Locate every blood parasite and identify its species.
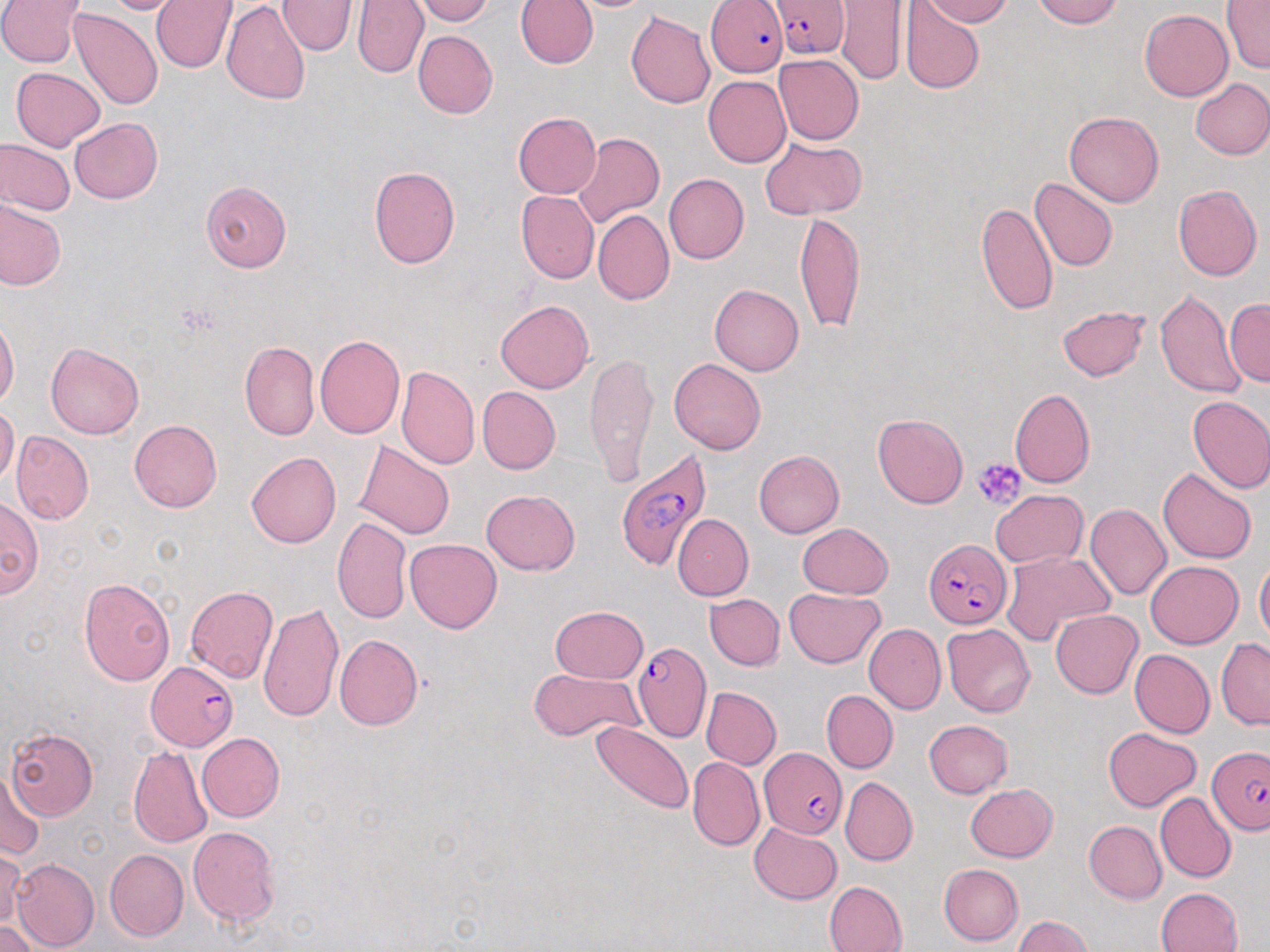
Approximate bounding boxes as named x1/y1/x2/y2 corners in pixels.
Plasmodium falciparum-infected red blood cells: (x1=770, y1=0, x2=849, y2=58), (x1=705, y1=1, x2=788, y2=77), (x1=614, y1=449, x2=712, y2=571), (x1=922, y1=538, x2=1014, y2=630), (x1=632, y1=641, x2=712, y2=742), (x1=143, y1=661, x2=240, y2=751), (x1=1207, y1=744, x2=1270, y2=834), (x1=759, y1=747, x2=845, y2=839).
No Plasmodium ovale, Plasmodium malariae, Plasmodium vivax, Babesia divergens, or Trypanosoma brucei observed.

Summary:
  - Uninfected red blood cell locations: (x1=0, y1=0, x2=84, y2=68), (x1=99, y1=0, x2=188, y2=15), (x1=152, y1=0, x2=237, y2=73), (x1=221, y1=0, x2=311, y2=105), (x1=278, y1=0, x2=359, y2=56), (x1=352, y1=0, x2=429, y2=78), (x1=412, y1=0, x2=493, y2=24), (x1=516, y1=0, x2=598, y2=69), (x1=920, y1=0, x2=1012, y2=27), (x1=1032, y1=0, x2=1120, y2=27), (x1=1220, y1=0, x2=1269, y2=74), (x1=836, y1=1, x2=909, y2=86), (x1=899, y1=1, x2=984, y2=95), (x1=68, y1=6, x2=163, y2=110), (x1=1140, y1=9, x2=1232, y2=101), (x1=626, y1=11, x2=716, y2=109), (x1=413, y1=30, x2=497, y2=119), (x1=774, y1=54, x2=865, y2=144), (x1=11, y1=67, x2=105, y2=150), (x1=703, y1=76, x2=792, y2=168), (x1=1191, y1=78, x2=1270, y2=160), (x1=1065, y1=111, x2=1163, y2=207), (x1=512, y1=112, x2=602, y2=199), (x1=70, y1=117, x2=162, y2=203), (x1=572, y1=132, x2=663, y2=228), (x1=0, y1=137, x2=75, y2=215), (x1=759, y1=137, x2=866, y2=219), (x1=368, y1=166, x2=461, y2=269), (x1=663, y1=173, x2=749, y2=264), (x1=1029, y1=178, x2=1118, y2=272), (x1=201, y1=181, x2=291, y2=271), (x1=1173, y1=184, x2=1262, y2=280), (x1=516, y1=190, x2=599, y2=284), (x1=0, y1=196, x2=65, y2=290), (x1=975, y1=202, x2=1058, y2=317), (x1=592, y1=209, x2=674, y2=306), (x1=795, y1=212, x2=865, y2=336), (x1=710, y1=284, x2=805, y2=376), (x1=1155, y1=288, x2=1245, y2=399), (x1=495, y1=299, x2=594, y2=393), (x1=1226, y1=300, x2=1270, y2=387), (x1=1056, y1=305, x2=1150, y2=381), (x1=0, y1=317, x2=19, y2=409), (x1=314, y1=335, x2=405, y2=439), (x1=239, y1=340, x2=319, y2=440), (x1=45, y1=343, x2=143, y2=439), (x1=584, y1=348, x2=659, y2=488), (x1=669, y1=358, x2=766, y2=455), (x1=396, y1=366, x2=479, y2=469), (x1=478, y1=386, x2=561, y2=473), (x1=1010, y1=388, x2=1095, y2=488), (x1=1187, y1=395, x2=1270, y2=494), (x1=0, y1=405, x2=19, y2=486), (x1=872, y1=413, x2=968, y2=508), (x1=129, y1=419, x2=223, y2=512), (x1=12, y1=431, x2=93, y2=525), (x1=355, y1=440, x2=456, y2=539), (x1=754, y1=449, x2=844, y2=537), (x1=246, y1=451, x2=341, y2=548), (x1=1158, y1=467, x2=1256, y2=564), (x1=481, y1=488, x2=580, y2=576), (x1=991, y1=489, x2=1088, y2=569), (x1=0, y1=497, x2=42, y2=599), (x1=1086, y1=503, x2=1172, y2=600), (x1=672, y1=514, x2=754, y2=600), (x1=332, y1=516, x2=411, y2=624), (x1=797, y1=523, x2=893, y2=598), (x1=405, y1=538, x2=501, y2=633), (x1=1001, y1=551, x2=1115, y2=644), (x1=1255, y1=556, x2=1270, y2=648), (x1=1145, y1=561, x2=1243, y2=648), (x1=78, y1=577, x2=175, y2=686), (x1=184, y1=586, x2=278, y2=684), (x1=784, y1=588, x2=884, y2=667), (x1=704, y1=593, x2=784, y2=670), (x1=258, y1=601, x2=344, y2=722), (x1=550, y1=605, x2=648, y2=684), (x1=1050, y1=609, x2=1142, y2=698), (x1=864, y1=623, x2=945, y2=714), (x1=943, y1=623, x2=1035, y2=717), (x1=334, y1=635, x2=422, y2=731), (x1=1216, y1=638, x2=1270, y2=729), (x1=1130, y1=649, x2=1214, y2=738), (x1=530, y1=668, x2=643, y2=741), (x1=701, y1=686, x2=781, y2=769), (x1=822, y1=690, x2=897, y2=773), (x1=924, y1=719, x2=1014, y2=798), (x1=591, y1=720, x2=694, y2=816), (x1=1103, y1=726, x2=1201, y2=811), (x1=7, y1=728, x2=97, y2=818), (x1=197, y1=731, x2=285, y2=822), (x1=128, y1=746, x2=212, y2=849), (x1=687, y1=757, x2=763, y2=851), (x1=2, y1=767, x2=46, y2=861), (x1=840, y1=777, x2=918, y2=865), (x1=965, y1=783, x2=1058, y2=861), (x1=1155, y1=792, x2=1236, y2=883), (x1=1083, y1=820, x2=1166, y2=904), (x1=750, y1=822, x2=842, y2=904), (x1=188, y1=826, x2=281, y2=928), (x1=0, y1=847, x2=24, y2=929), (x1=104, y1=848, x2=189, y2=941), (x1=11, y1=857, x2=99, y2=951), (x1=939, y1=863, x2=1023, y2=946), (x1=824, y1=881, x2=906, y2=952), (x1=1155, y1=887, x2=1242, y2=952), (x1=1011, y1=915, x2=1093, y2=952), (x1=0, y1=919, x2=41, y2=952)
  - Platelet locations: (x1=180, y1=303, x2=224, y2=337), (x1=974, y1=457, x2=1027, y2=510)
  - Slide-level diagnosis: Plasmodium falciparum
  - Magnification: 1000x
  - Preparation: thin blood smear
  - Image size: 1270×952 pixels
  - Modality: optical microscopy
  - Stain: May-Grünwald-Giemsa
  - Field of view: one of a larger specimen